Report the malaria status of this cell.
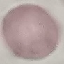

Uninfected.

{
  "image_type": "cell patch, automatically extracted from a larger field of view and resized to 64 × 64 pixels",
  "stain": "Giemsa",
  "capture": "smartphone through the microscope eyepiece",
  "preparation": "thin blood film"
}